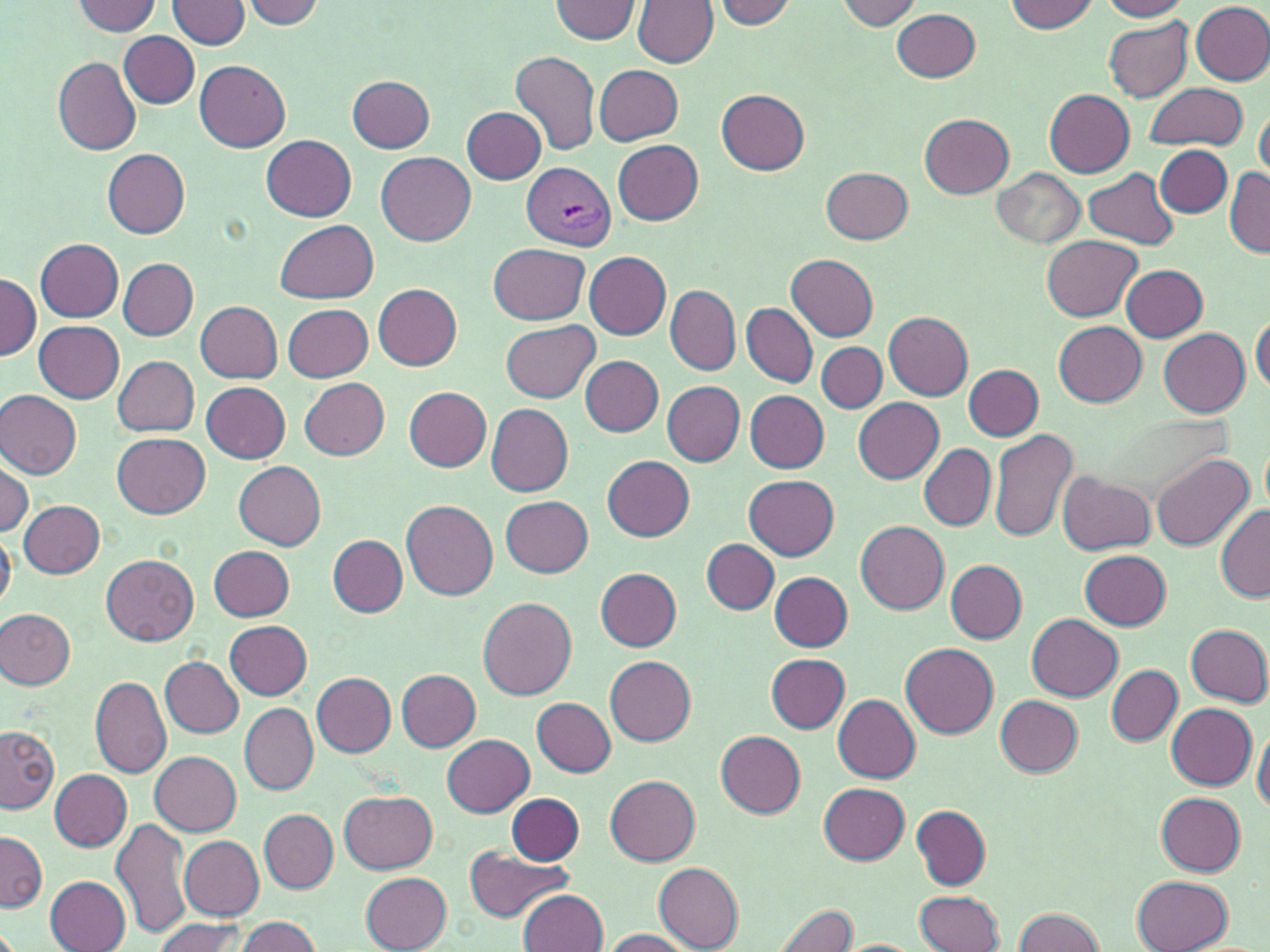
Summary:
  - Coordinate format: approximate bounding boxes as (x1,y1)-(x2,y2) corner pairs in pixels
  - Plasmodium vivax-infected red blood cell locations: (521,162)-(616,250)
  - Uninfected red blood cell locations: (549,0)-(642,43), (714,0)-(796,29), (1102,0)-(1188,20), (72,1)-(160,36), (170,1)-(251,49), (632,1)-(716,67), (834,1)-(922,29), (1004,1)-(1098,33), (242,2)-(323,28), (1190,3)-(1270,85), (892,9)-(980,82), (1103,16)-(1193,102), (119,31)-(200,107), (511,51)-(600,156), (53,56)-(142,154), (196,60)-(289,152), (594,64)-(684,146), (347,75)-(435,151), (1147,83)-(1244,151), (717,89)-(809,174), (1044,89)-(1133,176), (464,106)-(544,184), (1255,110)-(1269,181), (920,115)-(1013,198), (262,136)-(357,221), (613,140)-(703,225), (1155,145)-(1232,217), (103,149)-(190,238), (376,151)-(476,245), (821,166)-(913,245), (994,167)-(1085,249), (1084,167)-(1178,249), (1225,167)-(1269,258), (276,220)-(378,304), (1041,236)-(1142,320), (35,240)-(123,322), (488,243)-(588,325), (578,246)-(663,428), (585,251)-(671,340), (788,254)-(877,340), (119,258)-(198,339), (1120,264)-(1208,341), (0,274)-(39,362), (374,284)-(462,370), (665,286)-(739,375), (663,299)-(817,381), (195,302)-(283,383), (283,304)-(372,382), (743,304)-(817,387), (884,312)-(972,400), (1251,317)-(1269,393), (502,320)-(599,402), (1053,320)-(1146,407), (34,321)-(124,403), (1158,328)-(1250,417), (818,343)-(886,412), (114,356)-(199,436), (582,356)-(663,436), (964,364)-(1043,440), (301,377)-(390,460), (662,380)-(745,466), (202,381)-(289,462), (404,387)-(492,469), (1,389)-(82,480), (745,391)-(830,472), (853,397)-(944,483), (487,404)-(573,496), (989,428)-(1078,544), (113,433)-(209,518), (920,443)-(996,531), (1151,452)-(1253,551), (602,455)-(695,541), (0,457)-(34,536), (233,460)-(326,549), (1059,472)-(1155,555), (743,474)-(839,560), (500,495)-(594,576), (20,500)-(104,578), (402,500)-(498,599), (1216,504)-(1269,601), (854,520)-(949,614), (0,530)-(16,612), (329,535)-(407,617), (702,539)-(779,613), (208,546)-(294,621), (1080,550)-(1171,630), (101,554)-(198,645), (947,560)-(1027,642), (596,568)-(683,651), (770,571)-(852,652), (479,595)-(577,699), (0,607)-(74,688), (1027,614)-(1121,700), (223,620)-(313,699), (1186,624)-(1270,706), (900,643)-(999,737), (764,654)-(850,732), (160,656)-(244,738), (605,656)-(696,746), (1107,665)-(1181,745), (398,670)-(480,749), (311,672)-(396,755), (90,676)-(172,777), (834,694)-(921,783), (996,695)-(1082,776), (532,697)-(617,776), (240,703)-(318,795), (1167,703)-(1257,788), (1,726)-(59,813), (1252,727)-(1270,814), (715,731)-(805,817), (442,733)-(534,816), (150,751)-(242,834), (49,769)-(132,850), (605,774)-(701,865), (818,782)-(910,863), (340,790)-(436,872), (507,792)-(584,864), (1157,792)-(1247,876), (911,804)-(991,889), (259,809)-(338,892), (112,817)-(192,940), (0,830)-(46,913), (178,834)-(265,919), (464,845)-(574,921), (653,864)-(744,952), (360,872)-(452,951), (1132,874)-(1232,952), (46,875)-(132,951), (914,889)-(1004,951), (519,890)-(609,952), (774,902)-(859,952), (1010,907)-(1107,952), (229,916)-(323,952), (152,919)-(248,952), (600,928)-(694,951)
  - Slide-level diagnosis: Plasmodium vivax
  - Modality: light microscopy
  - Field of view: single
  - Preparation: thin blood smear
  - Magnification: 1000x
  - Stain: May-Grünwald-Giemsa
  - Image size: 1270×952 pixels